Assess this cell for malaria.
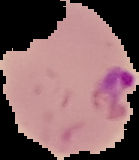

Parasitized.

Summary:
  - Image size: 139×160 pixels
  - Preparation: thin blood film
  - Image type: cell region segmented out of the field of view; surrounding area masked to black